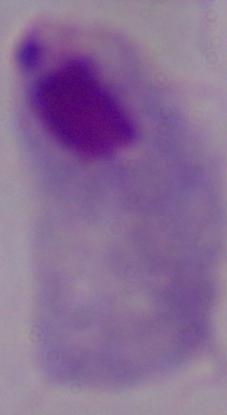

Summary:
  - Identification: trichomonad
  - Modality: photomicrograph
  - Magnification: 1000x